Point out each Plasmodium parasite.
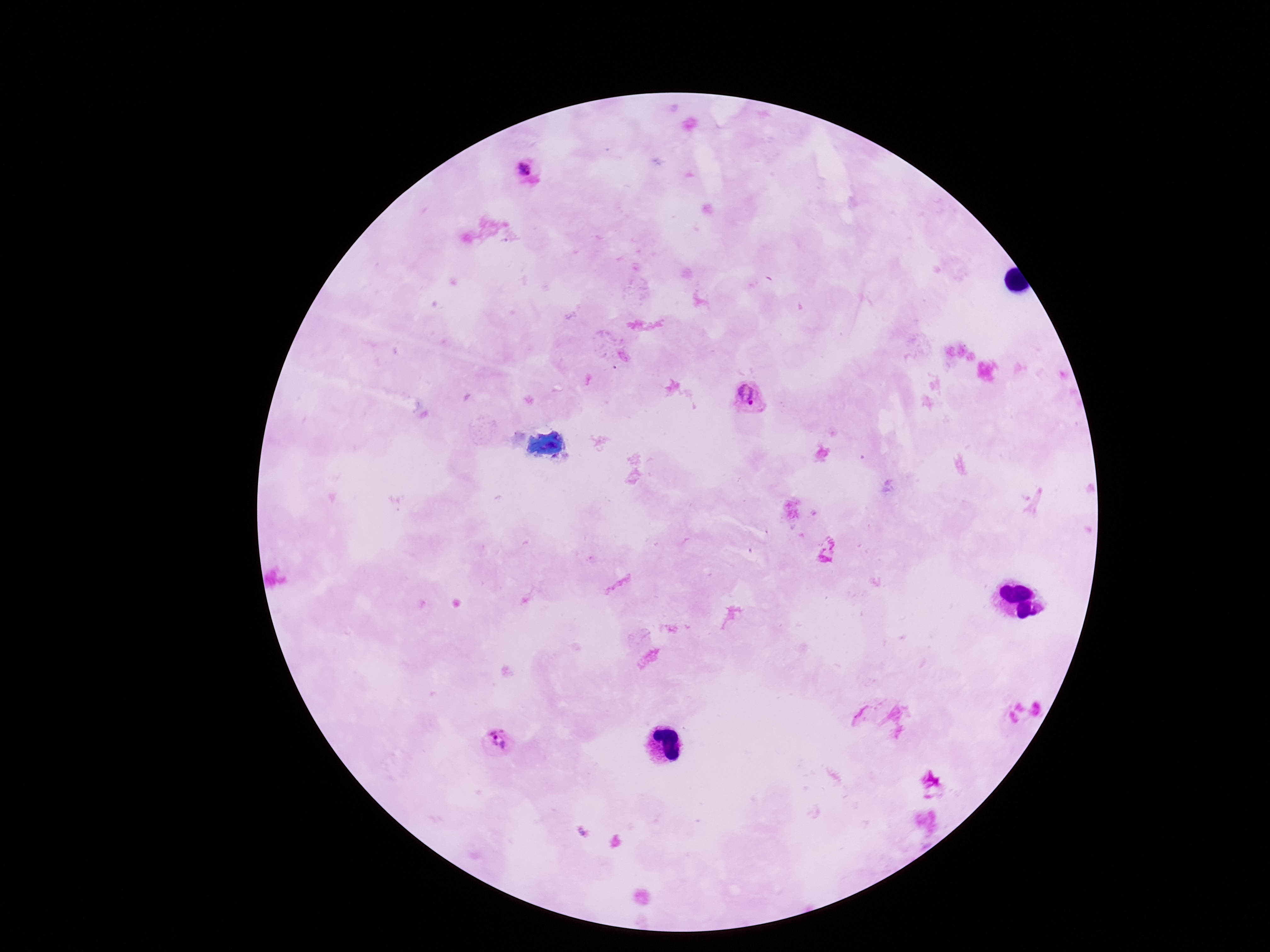

Approximate object centers, in pixels from the top-left corner.
Plasmodium parasites: (x=532, y=176), (x=747, y=395), (x=1022, y=713), (x=500, y=741).

Summary:
  - Capture: smartphone camera through the microscope eyepiece
  - Preparation: thick blood film
  - Patient malaria status: infected
  - Field of view: one from this slide
  - Stain: Giemsa
  - Magnification: 100x
  - Image size: 1270×952 pixels